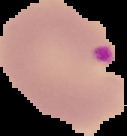 Image is 127×136 pixels. Cell region segmented out of the field of view; the surrounding area is masked to black. Result: malaria parasites identified. From a thin blood smear.